Comment on the morphology of the red blood cells.
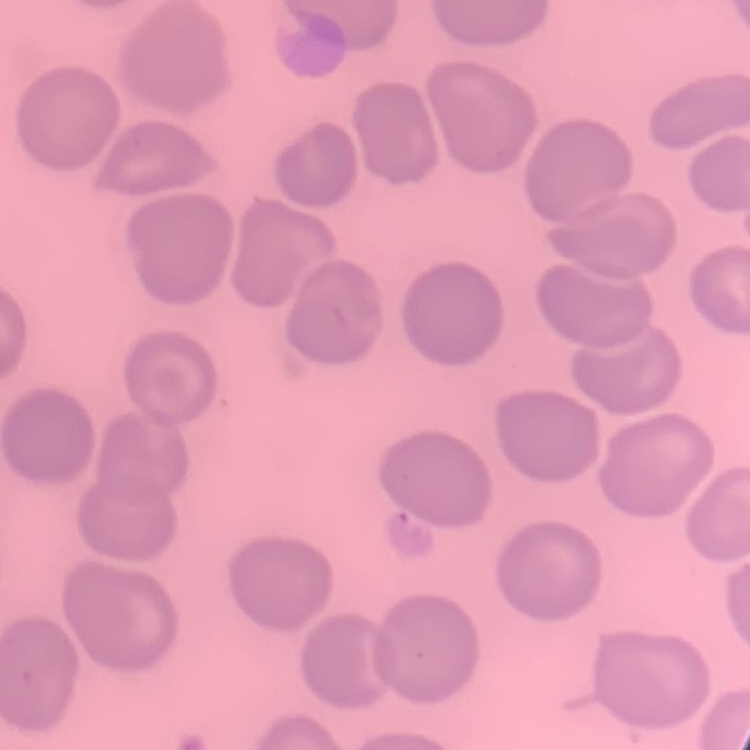
They show no rouleaux formation.

Summary:
  - Image type: square crop of a larger photomicrograph
  - Preparation: thin blood film
  - Stain: Field's or Giemsa